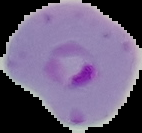
Summary:
  - Result: Plasmodium parasites identified
  - Preparation: thin blood film
  - Image size: 142×133 pixels
  - Image type: segmented cell region with the area outside set to black